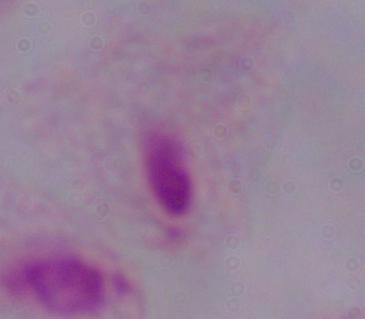
Summary:
  - Modality: micrograph
  - Identification: trichomonad
  - Magnification: 1000x